Assess this cell for malaria.
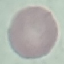
It is uninfected.

Summary:
  - Image type: automatically extracted cell patch, resized to 64 × 64 pixels
  - Capture: smartphone camera at the microscope eyepiece
  - Stain: Giemsa
  - Preparation: thin smear